State which parasite is depicted.
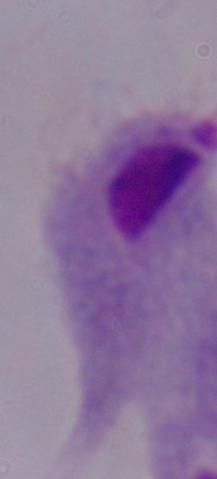

This is a trichomonad.

Summary:
  - Modality: photomicrograph
  - Magnification: 1000x